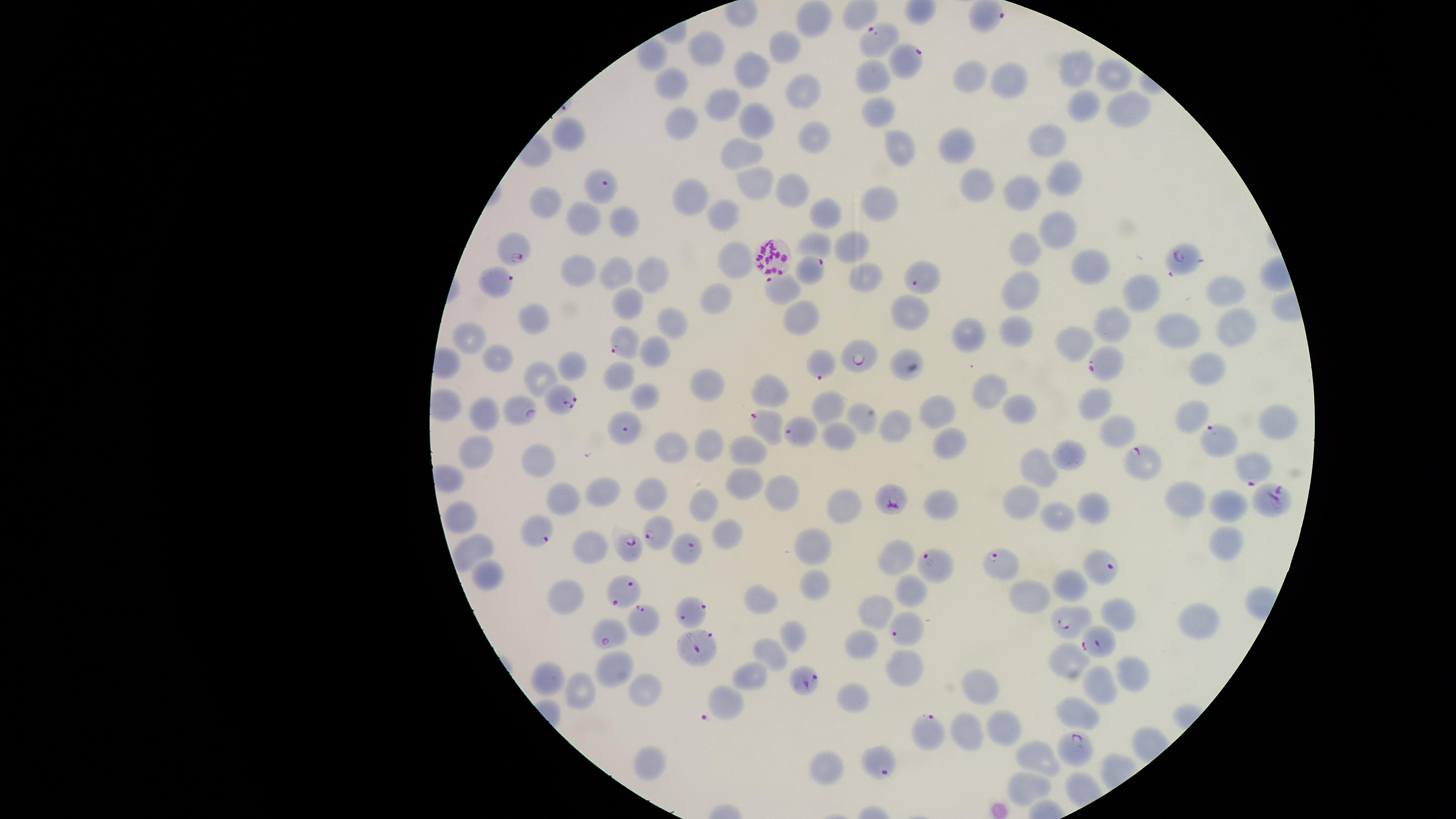

preparation = thin blood smear
stain = Giemsa
parasitized RBCs = approximate marker points as [x, y] in pixels: [874, 39], [903, 62], [600, 188], [513, 248], [1184, 257], [772, 260], [811, 270], [921, 276], [498, 284], [626, 343], [858, 356], [1101, 364], [819, 366], [561, 400], [523, 409], [766, 426], [626, 429], [802, 433], [1217, 440], [1142, 460], [1253, 468], [894, 498], [1267, 502], [540, 530], [657, 532], [627, 544], [687, 549], [997, 561], [938, 563], [1096, 568], [620, 594], [691, 610], [1063, 620], [643, 622], [901, 629], [608, 633], [1100, 648], [700, 651], [803, 680], [925, 732], [1074, 750], [873, 761]
uninfected RBCs = approximate marker points as [x, y] in pixels: [811, 20], [703, 50], [786, 50], [1081, 69], [751, 72], [1116, 73], [871, 76], [971, 77], [674, 83], [1011, 83], [798, 90], [718, 101], [1085, 105], [875, 109], [1124, 111], [757, 118], [682, 121], [813, 135], [569, 136], [1053, 140], [960, 146], [899, 148], [743, 151], [1061, 174], [751, 182], [790, 186], [973, 188], [1021, 193], [692, 198], [543, 202], [878, 205], [722, 210], [826, 211], [625, 219], [580, 220], [1055, 229], [850, 243], [815, 246], [1024, 251], [732, 260], [1089, 265], [576, 269], [618, 273], [647, 273], [859, 277], [1019, 288], [1139, 288], [1224, 288], [783, 291], [625, 301], [710, 301], [913, 309], [796, 315], [527, 318], [1117, 319], [673, 322], [1235, 322], [1175, 332], [1015, 336], [471, 338], [1078, 338], [970, 343], [653, 351], [899, 357], [498, 362], [571, 366], [1209, 369], [626, 376], [542, 378], [704, 388], [772, 393], [988, 394], [644, 397], [1097, 402], [828, 407], [939, 409], [1018, 412], [481, 414], [861, 418], [1187, 418], [1278, 423], [897, 425], [1117, 430], [833, 437], [952, 441], [671, 445], [710, 447], [748, 448], [1069, 453], [475, 455], [533, 462], [1034, 466], [741, 482], [783, 489], [598, 490], [651, 492], [562, 497], [1192, 497], [1228, 498], [1025, 499], [944, 500], [844, 502], [704, 504], [1093, 508], [457, 516], [1057, 517], [722, 538], [1223, 543], [584, 547], [811, 547], [465, 550], [895, 552], [486, 574], [814, 585], [1067, 588], [905, 590], [1032, 593], [757, 602], [875, 613], [1113, 613], [1196, 619], [790, 635], [860, 643], [772, 652], [1073, 659], [615, 667], [905, 667], [749, 677], [1131, 677], [551, 678], [639, 688], [580, 690], [1097, 691], [978, 695], [723, 701], [853, 701], [1080, 713], [1004, 717], [960, 730], [1036, 757], [646, 761], [825, 771], [1024, 784]
image size = 1456×819 pixels
presence = malaria parasites detected
capture = smartphone photograph through the microscope eyepiece
visible region = circular
field of view = single
species = Plasmodium falciparum